Locate every malaria parasite and every leukocyte.
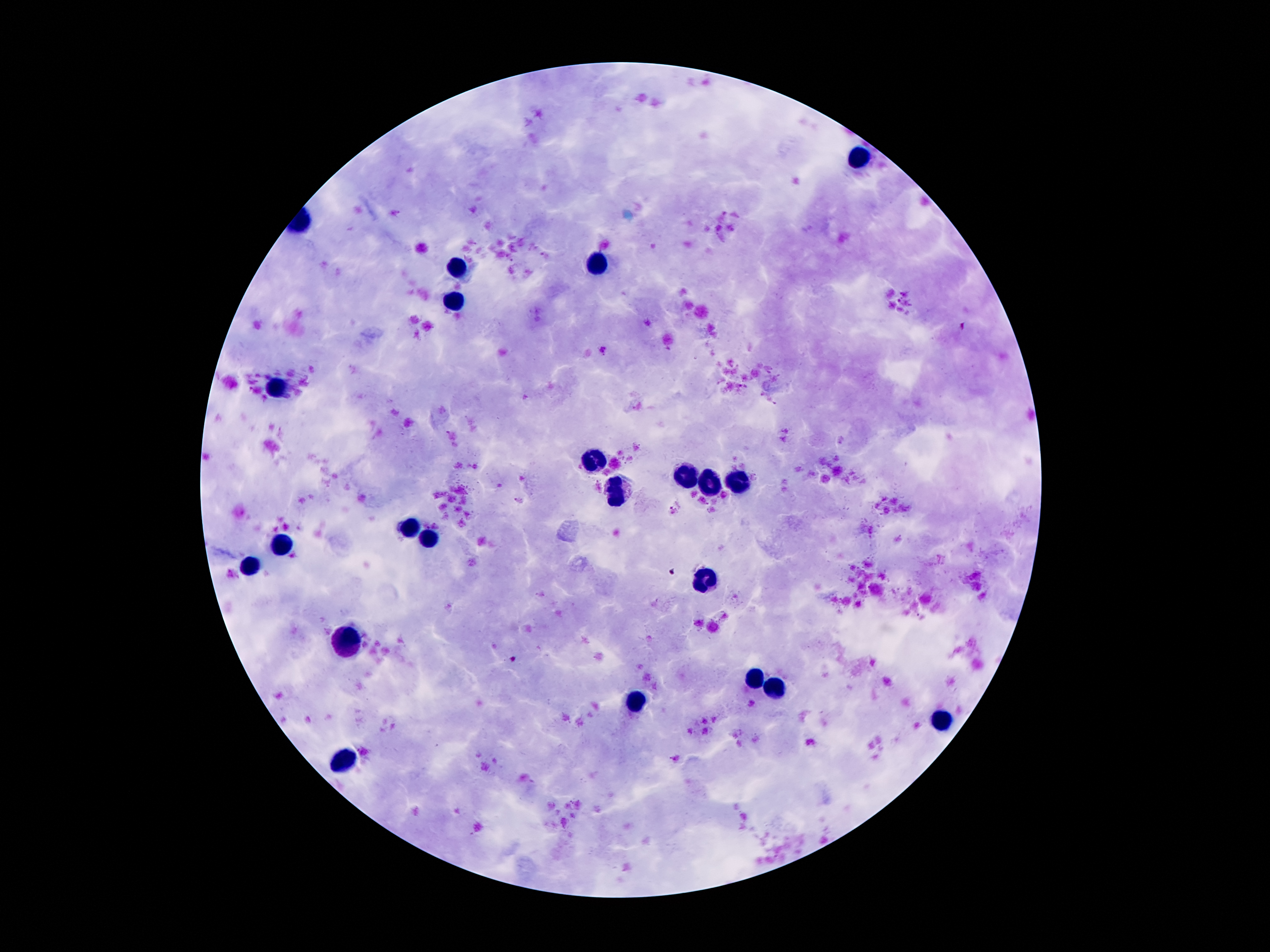
Approximate centers as [x, y] in pixels.
Malaria parasites: [604, 350], [671, 511], [672, 573], [514, 659].
Leukocytes: [858, 158], [599, 264], [457, 268], [453, 301], [276, 387], [591, 462], [684, 476], [737, 480], [711, 486], [617, 490], [406, 527], [431, 538], [281, 546], [249, 564], [709, 580], [345, 642], [752, 679], [774, 689], [634, 702], [940, 719], [339, 758].

Patient malaria status: infected with Plasmodium falciparum. Photographed through the microscope eyepiece with a smartphone camera. 100x magnification. Giemsa-stained preparation. Image is 1270×952 pixels. Thick blood film. Single field of view.